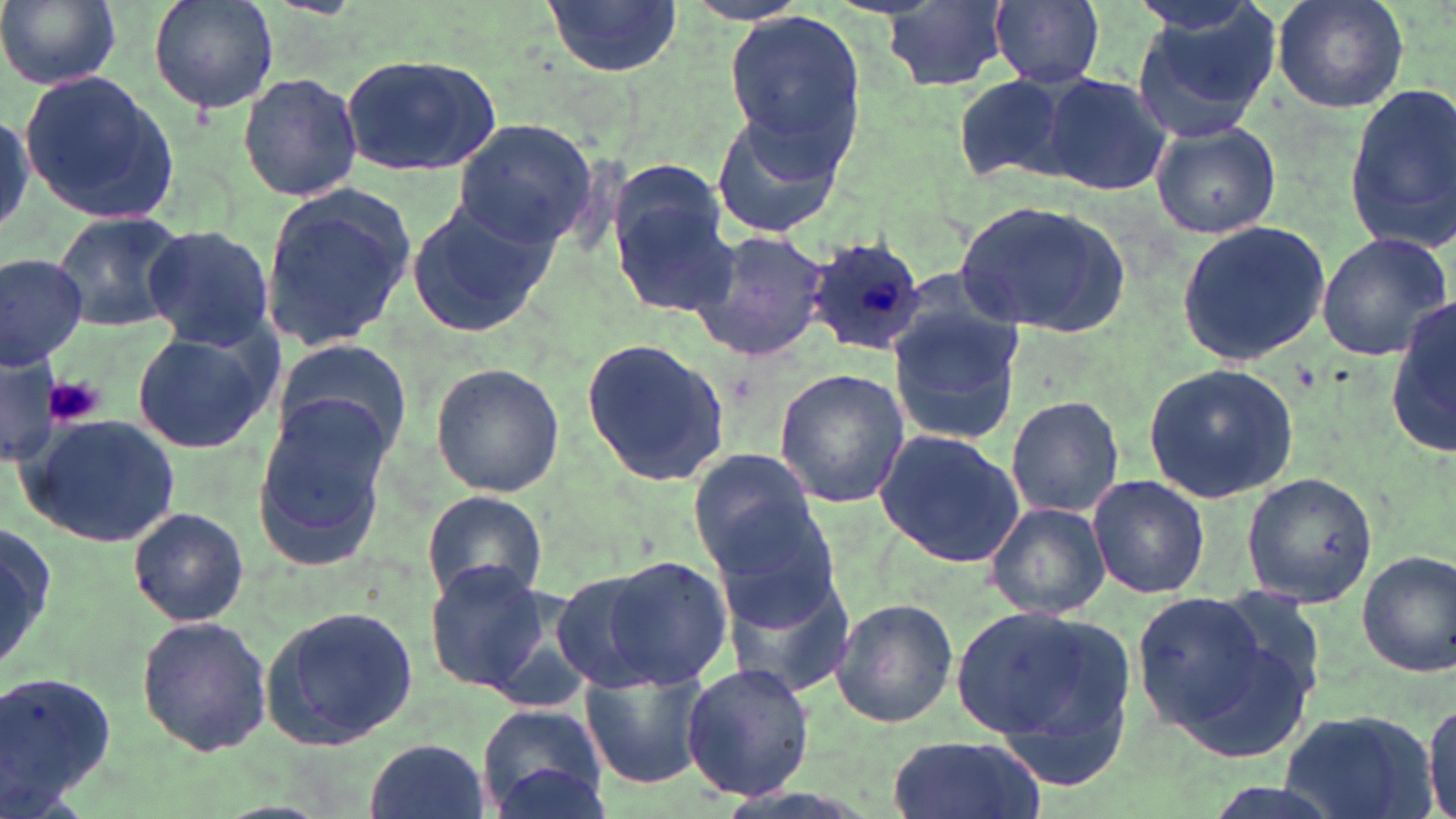

Approximate bounding boxes as [x1, y1, x2, y2] in pixels. Uninfected red blood cell locations: [0, 0, 121, 91], [149, 0, 280, 114], [542, 0, 684, 77], [989, 0, 1104, 88], [1270, 0, 1409, 114], [881, 2, 1015, 91], [1128, 7, 1278, 145], [723, 12, 870, 155], [339, 55, 503, 176], [237, 70, 363, 204], [1041, 71, 1173, 197], [949, 72, 1082, 184], [21, 73, 180, 225], [1347, 80, 1456, 250], [713, 111, 844, 239], [450, 119, 599, 250], [1150, 121, 1281, 240], [610, 178, 734, 313], [257, 184, 416, 355], [403, 198, 551, 339], [955, 199, 1131, 338], [48, 210, 189, 331], [1174, 221, 1332, 364], [142, 224, 274, 351], [687, 228, 832, 362], [1314, 232, 1453, 362], [0, 252, 89, 371], [1388, 297, 1455, 456], [888, 299, 1024, 448], [129, 327, 279, 455], [581, 335, 732, 489], [270, 337, 411, 465], [0, 356, 61, 469], [430, 363, 563, 499], [1141, 363, 1298, 504], [774, 369, 910, 509], [252, 392, 395, 568], [1006, 395, 1124, 518], [21, 414, 181, 548], [874, 428, 1026, 569], [688, 450, 825, 569], [1241, 469, 1381, 608], [1088, 473, 1210, 600], [421, 490, 547, 603], [704, 499, 841, 632], [984, 501, 1111, 619], [129, 507, 250, 625], [0, 519, 58, 680], [1356, 548, 1456, 680], [600, 556, 735, 689], [424, 562, 551, 693], [723, 569, 858, 702], [551, 570, 670, 692], [1129, 588, 1308, 748], [831, 598, 958, 728], [954, 601, 1139, 784], [259, 604, 422, 750], [137, 614, 272, 757], [578, 662, 712, 790], [681, 662, 815, 802], [2, 664, 118, 810], [1423, 697, 1456, 819], [473, 703, 609, 819], [1278, 706, 1435, 819], [888, 732, 1041, 819], [366, 735, 487, 819], [491, 761, 612, 818]. Plasmodium ovale-infected red blood cell locations: [806, 236, 929, 357]. Platelet locations: [48, 376, 107, 426]. Slide-level diagnosis: Plasmodium ovale. Image is 1456×819 pixels. Thin blood smear. Captured at 1000x magnification. One field of a larger specimen. Optical microscopy. May-Grünwald-Giemsa stain.